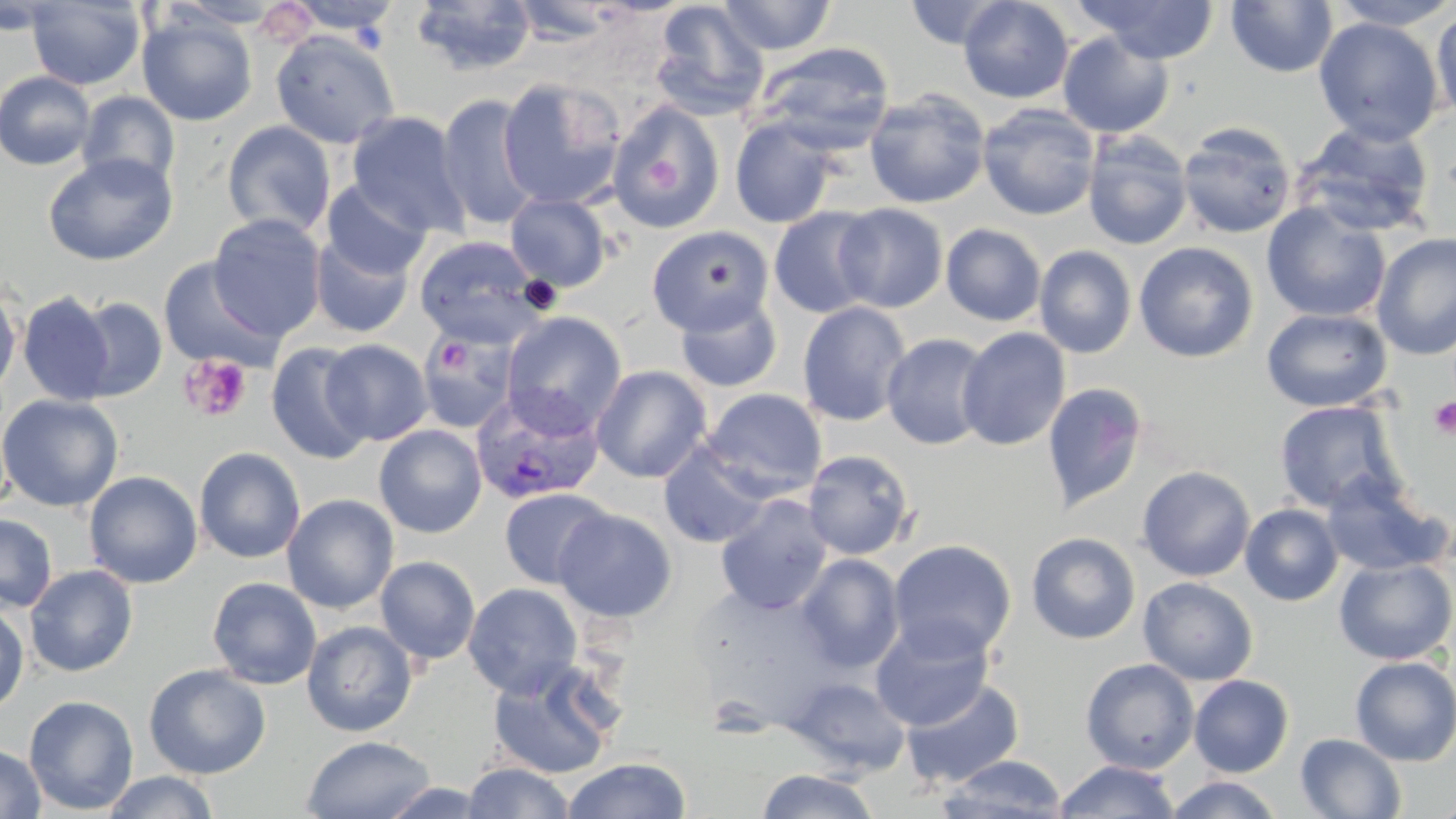

Approximate bounding boxes as (x1,y1)-(x2,y2) corner pairs in pixels. Uninfected red blood cell locations: (0,0)-(67,36), (164,0)-(289,29), (718,0)-(836,55), (958,0)-(1074,104), (1075,0)-(1220,64), (1225,0)-(1339,78), (1329,0)-(1456,30), (26,1)-(146,90), (285,1)-(402,35), (411,1)-(536,76), (904,1)-(1012,49), (508,2)-(628,46), (650,2)-(770,121), (1430,6)-(1456,126), (137,12)-(257,126), (1313,16)-(1444,146), (271,31)-(400,148), (1057,32)-(1174,139), (755,42)-(894,150), (0,70)-(96,170), (497,76)-(626,211), (864,89)-(991,209), (76,91)-(181,191), (437,93)-(542,232), (607,101)-(724,233), (977,102)-(1101,221), (346,111)-(471,239), (730,118)-(839,228), (1293,119)-(1436,238), (222,121)-(336,238), (1177,121)-(1298,239), (1082,130)-(1193,251), (43,153)-(177,266), (322,180)-(432,280), (505,192)-(612,292), (1261,202)-(1391,323), (833,203)-(948,313), (769,207)-(881,318), (207,214)-(327,340), (941,223)-(1046,326), (646,225)-(773,337), (310,232)-(416,339), (1372,232)-(1456,360), (414,235)-(544,347), (1133,241)-(1259,362), (1034,245)-(1137,358), (157,256)-(283,373), (0,284)-(22,399), (18,292)-(115,406), (674,293)-(782,393), (72,296)-(168,401), (797,301)-(912,426), (1261,307)-(1392,412), (501,311)-(627,435), (956,327)-(1071,451), (418,333)-(517,435), (882,333)-(993,450), (321,339)-(433,445), (267,341)-(374,465), (591,365)-(712,483), (1041,382)-(1148,512), (702,389)-(827,498), (0,394)-(123,512), (1274,400)-(1405,515), (374,425)-(487,538), (657,443)-(774,549), (194,447)-(306,563), (802,449)-(916,560), (1136,465)-(1256,581), (84,470)-(202,588), (1321,474)-(1451,577), (499,487)-(613,590), (282,494)-(399,614), (716,495)-(833,615), (1240,504)-(1344,606), (553,507)-(677,623), (0,514)-(57,612), (1026,532)-(1141,644), (888,539)-(1017,661), (795,553)-(905,673), (375,555)-(481,665), (1333,558)-(1455,665), (24,564)-(138,677), (207,577)-(322,689), (1138,577)-(1259,685), (463,582)-(582,697), (689,585)-(842,729), (0,604)-(29,713), (870,617)-(995,731), (301,620)-(417,737), (1350,655)-(1456,766), (486,658)-(623,780), (1080,658)-(1200,774), (144,664)-(271,779), (1188,674)-(1294,777), (785,676)-(911,776), (900,676)-(1025,789), (23,695)-(139,815), (1295,733)-(1407,818), (302,734)-(436,819), (0,743)-(46,819), (936,754)-(1068,818), (560,757)-(692,818), (1054,760)-(1180,817), (461,761)-(576,818), (756,769)-(880,819), (101,770)-(219,819), (1165,775)-(1286,818), (380,781)-(492,818), (1428,795)-(1456,818). Plasmodium vivax-infected red blood cell locations: (470,386)-(605,505). Platelet locations: (646,157)-(685,195), (433,338)-(471,375), (180,354)-(253,423), (1427,396)-(1456,439). Slide-level diagnosis: Plasmodium vivax. May-Grünwald-Giemsa stain. 1000x magnification. Thin blood smear. Image is 1456×819 pixels. Optical microscopy. One field of a larger specimen.